Locate platelets.
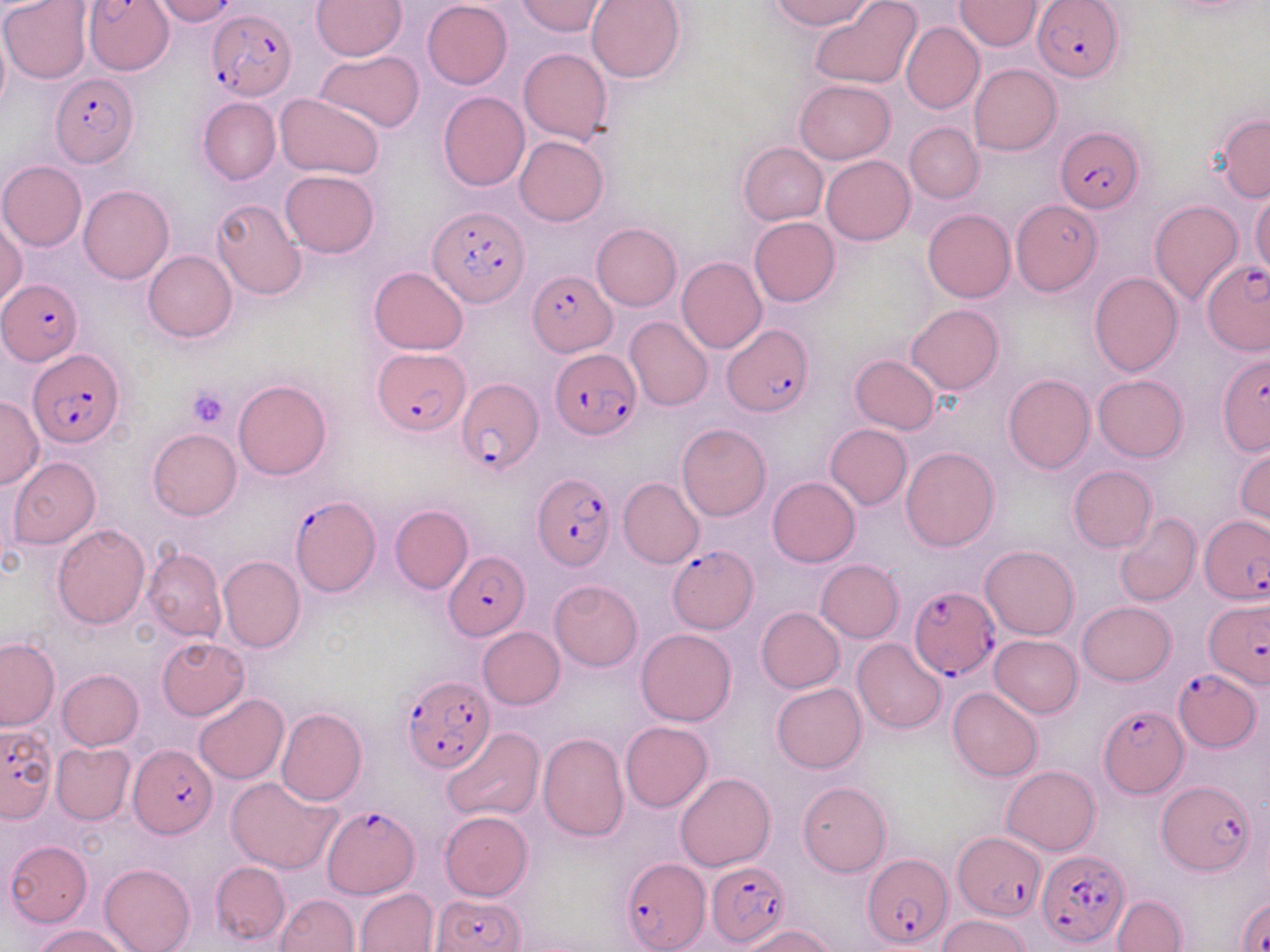

Approximate bounding boxes as [x1, y1, x2, y2] in pixels.
Platelets: [186, 384, 231, 428].

{
  "slide_level_diagnosis": "Plasmodium falciparum",
  "modality": "light microscopy",
  "image_size": "1270×952 pixels",
  "magnification": "1000x",
  "plasmodium_falciparum_infected_red_blood_cell_locations": "approximate bounding boxes as [x1, y1, x2, y2] in pixels: [85, 0, 173, 75], [1033, 3, 1122, 80], [207, 9, 295, 101], [50, 74, 140, 168], [1055, 126, 1143, 214], [429, 204, 528, 307], [1201, 258, 1268, 355], [527, 269, 616, 355], [1, 279, 82, 366], [721, 324, 814, 414], [29, 349, 124, 447], [373, 349, 471, 435], [550, 350, 641, 440], [1218, 352, 1270, 453], [456, 376, 542, 478], [531, 472, 617, 575], [289, 496, 380, 597], [1200, 516, 1267, 603], [668, 547, 759, 633], [444, 551, 528, 639], [909, 585, 1001, 679], [1204, 598, 1270, 686], [1174, 669, 1260, 751], [401, 675, 495, 773], [1097, 705, 1186, 799], [1, 723, 58, 822], [130, 742, 216, 840], [1155, 780, 1256, 876], [322, 803, 418, 899], [954, 832, 1044, 919], [1037, 849, 1128, 949], [861, 853, 949, 950], [619, 858, 709, 952], [706, 860, 791, 948], [1235, 894, 1270, 951], [433, 895, 527, 952]",
  "preparation": "thin blood film",
  "field_of_view": "one of a larger specimen",
  "stain": "May-Grünwald-Giemsa",
  "uninfected_red_blood_cell_locations": "approximate bounding boxes as [x1, y1, x2, y2] in pixels: [311, 0, 406, 60], [421, 0, 512, 89], [515, 0, 608, 36], [586, 0, 686, 83], [768, 0, 875, 30], [0, 1, 92, 84], [809, 1, 923, 89], [955, 1, 1043, 51], [900, 21, 983, 115], [0, 26, 10, 121], [518, 48, 613, 146], [314, 49, 424, 134], [969, 64, 1061, 154], [794, 80, 896, 164], [438, 90, 529, 191], [275, 92, 384, 180], [198, 97, 281, 184], [1215, 115, 1269, 201], [904, 122, 984, 204], [514, 136, 608, 226], [738, 142, 828, 225], [821, 155, 915, 244], [1, 161, 86, 251], [280, 170, 379, 259], [79, 185, 173, 283], [1249, 190, 1270, 276], [211, 198, 308, 300], [1148, 199, 1244, 305], [1012, 200, 1101, 294], [922, 208, 1015, 302], [748, 216, 840, 306], [0, 220, 26, 307], [592, 223, 681, 310], [144, 250, 236, 342], [677, 257, 766, 354], [368, 267, 469, 354], [1089, 272, 1183, 375], [907, 303, 1004, 394], [624, 317, 714, 411], [849, 355, 939, 433], [1003, 374, 1095, 474], [1093, 374, 1187, 462], [233, 379, 330, 480], [0, 394, 44, 488], [677, 423, 771, 521], [825, 424, 911, 509], [147, 428, 241, 520], [1234, 445, 1269, 528], [901, 447, 999, 551], [8, 457, 101, 549], [1068, 466, 1156, 552], [766, 477, 860, 567], [619, 478, 704, 568], [390, 506, 473, 594], [1115, 514, 1201, 607], [53, 524, 150, 629], [980, 545, 1078, 640], [143, 548, 226, 642], [217, 556, 305, 654], [816, 559, 903, 642], [549, 579, 643, 671], [1077, 601, 1175, 685], [756, 607, 844, 692], [478, 626, 565, 708], [635, 629, 737, 726], [990, 635, 1083, 717], [0, 638, 59, 730], [157, 638, 248, 718], [852, 638, 947, 735], [57, 669, 143, 750], [771, 682, 867, 773], [948, 687, 1043, 782], [194, 694, 289, 784], [276, 708, 367, 806], [620, 720, 713, 812], [443, 728, 544, 823], [538, 732, 628, 842], [51, 743, 135, 824], [1003, 765, 1099, 854], [675, 772, 775, 870], [226, 779, 340, 874], [798, 781, 890, 877], [439, 810, 533, 900], [5, 840, 92, 927], [210, 861, 290, 946], [99, 862, 195, 952], [356, 888, 438, 952], [276, 893, 359, 952], [1112, 895, 1186, 952], [939, 914, 1031, 952], [35, 924, 132, 952], [740, 925, 837, 952]"
}